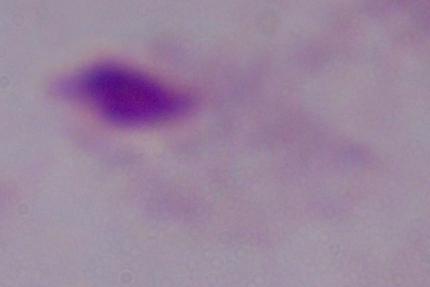

magnification = 1000x
identification = trichomonad
modality = micrograph